Assess this cell for malaria.
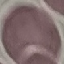
Uninfected.

Summary:
  - Capture: smartphone through the microscope eyepiece
  - Stain: Giemsa
  - Preparation: thin blood film
  - Image type: cell patch, automatically extracted from a larger field of view and resized to 64 × 64 pixels